Assess this cell for malaria.
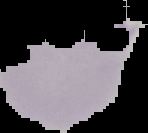

Parasitized.

From a thin blood smear. Cell region segmented out of the field of view; the surrounding area is masked to black. Image is 148×133 pixels.